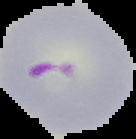 From a thin blood film. The area outside the segmented cell region is set to black. Malaria status: parasitized. Image is 136×139 pixels.